Assess the morphology of the red blood cells.
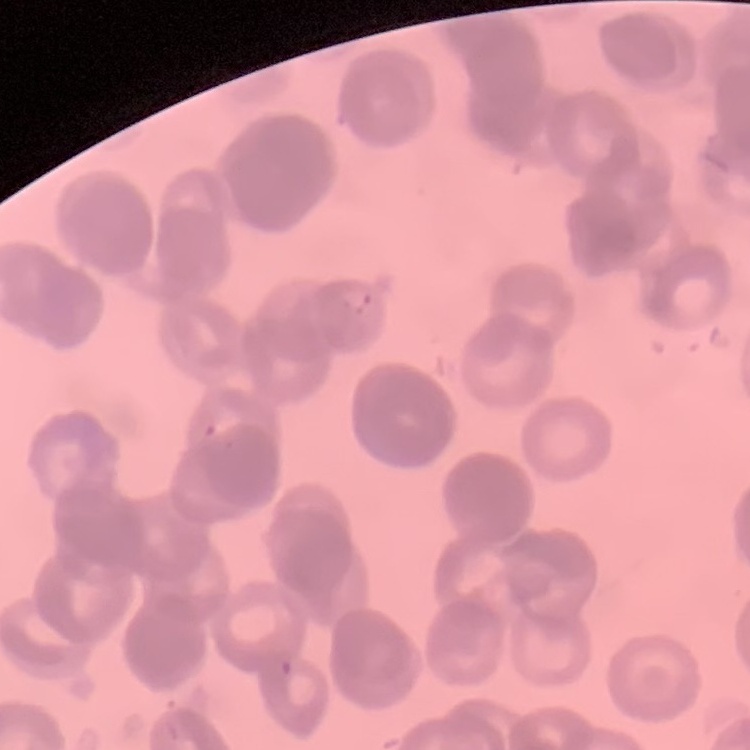

They show rouleaux formation.

{
  "stain": "Field's or Giemsa",
  "preparation": "thin blood smear",
  "image_type": "one tile cut from a larger photomicrograph"
}